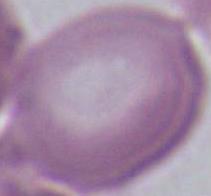

modality = micrograph
magnification = 1000x
identification = erythrocyte